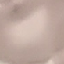
result: no malaria parasites seen
stain: Giemsa
preparation: thin blood film
image_type: cell patch, automatically extracted from a larger field of view and resized to 64 × 64 pixels
capture: smartphone through the microscope eyepiece